Rate the background quality.
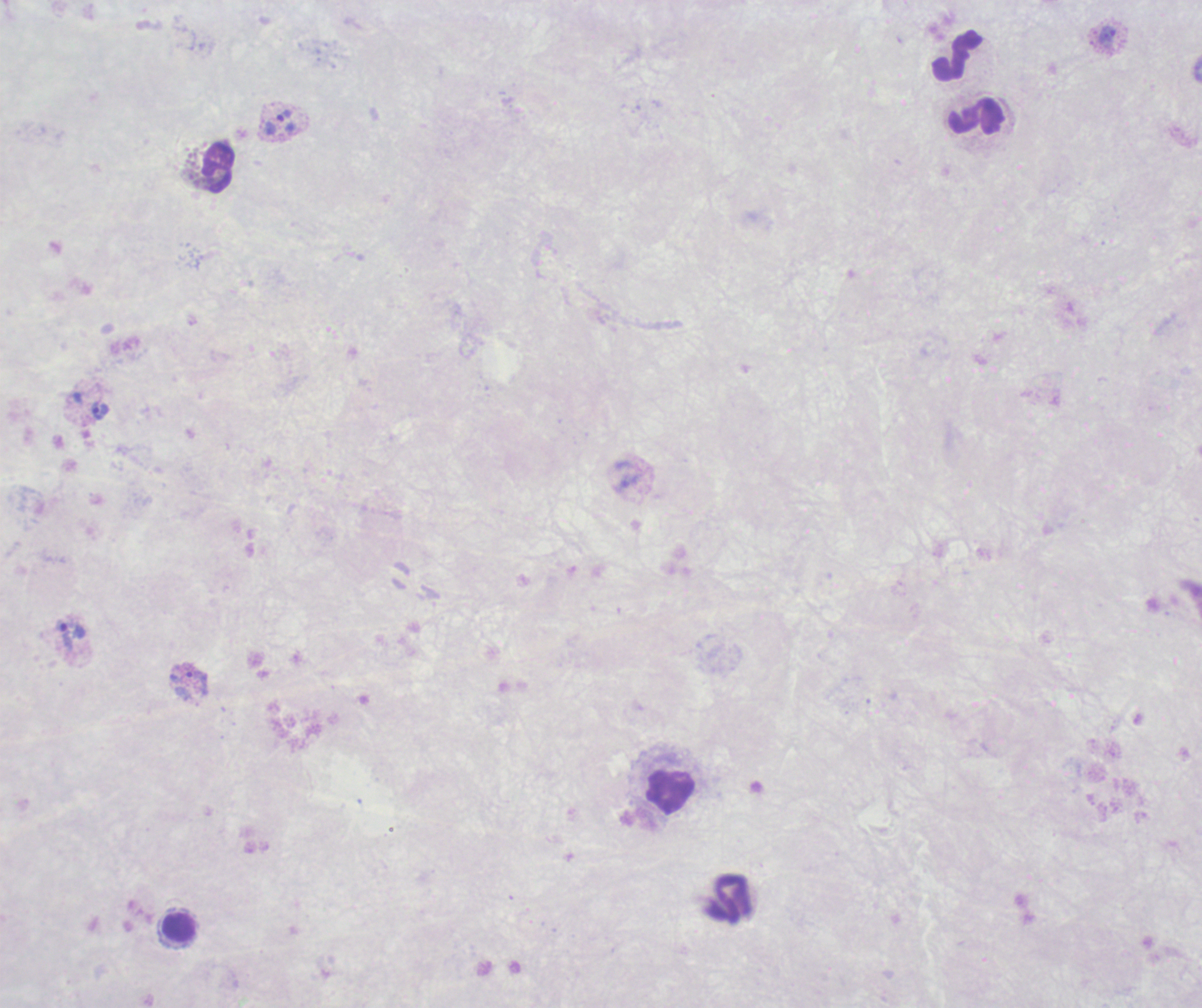
It is poor.

Approximate centers as {x, y} in pixels.
Summary:
  - Leukocyte locations: {956, 56}, {975, 117}, {218, 168}, {671, 792}, {729, 899}, {178, 927}
  - Trophozoite locations: {1108, 36}, {285, 115}, {99, 410}, {71, 635}, {197, 682}
  - Preparation: thick blood smear
  - Result: Plasmodium parasites identified
  - Context: previously used in an actual diagnosis
  - Image size: 1202×1008 pixels
  - Field of view: one from this slide
  - Magnification: 100x
  - Stain: Romanowsky
  - Coloration quality: bad